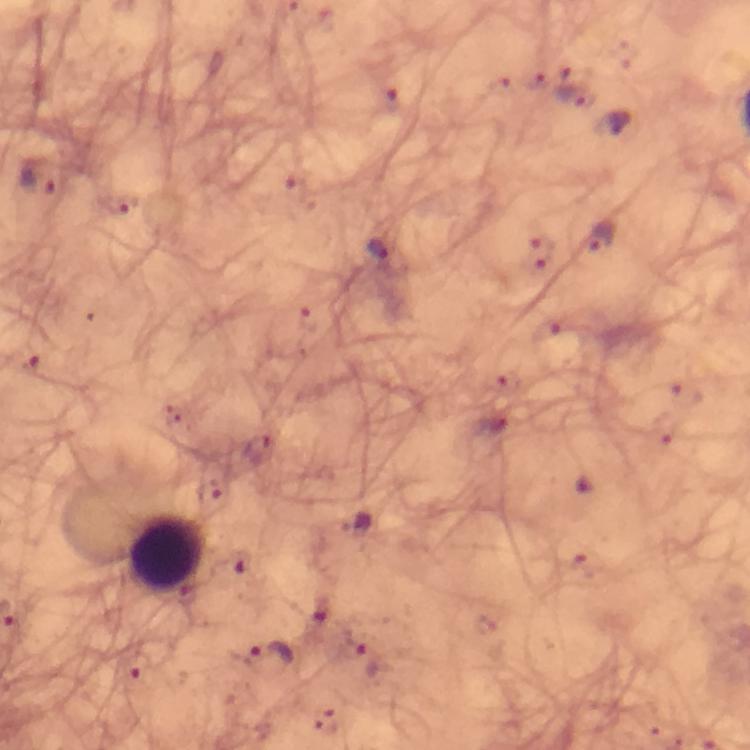
context = from a malaria diagnostic workup
preparation = thick blood film
stain = Giemsa
cropped from = a single field of view
leukocyte locations = approximate centers as [x, y] in pixels: [169, 554]
immersion oil = applied
malaria parasite locations = approximate centers as [x, y] in pixels: [39, 181], [120, 205], [601, 237], [378, 249], [30, 365], [271, 656]
image size = 750×750 pixels
capture = smartphone camera through the microscope
magnification = 100x